Describe the morphology of the erythrocytes.
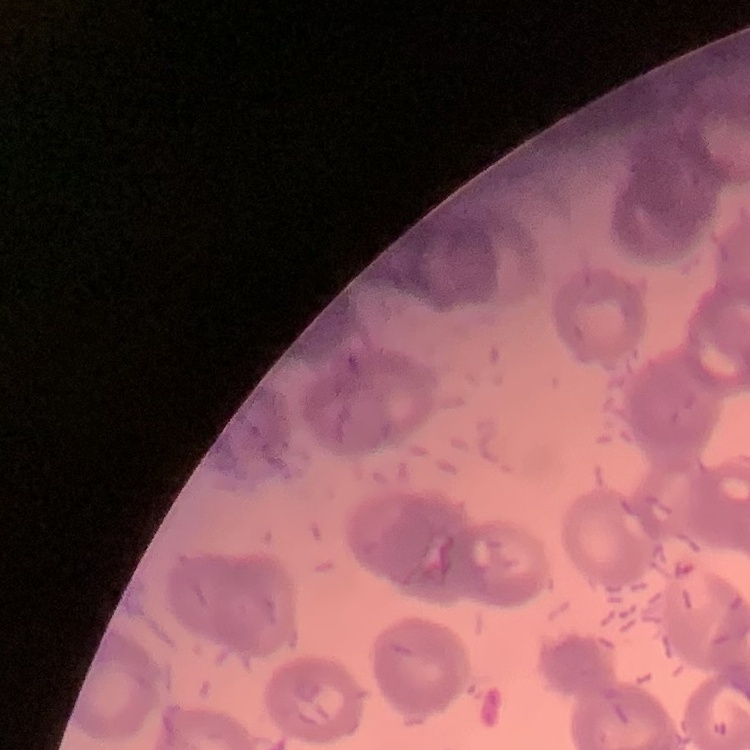

They show rouleaux formation.

preparation: thin blood smear
image_type: one tile cut from a larger photomicrograph
stain: Field's or Giemsa